Report the malaria status of this cell.
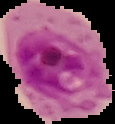
It is parasitized.

Summary:
  - Image type: segmented cell region on a black background
  - Image size: 115×124 pixels
  - Preparation: thin blood smear